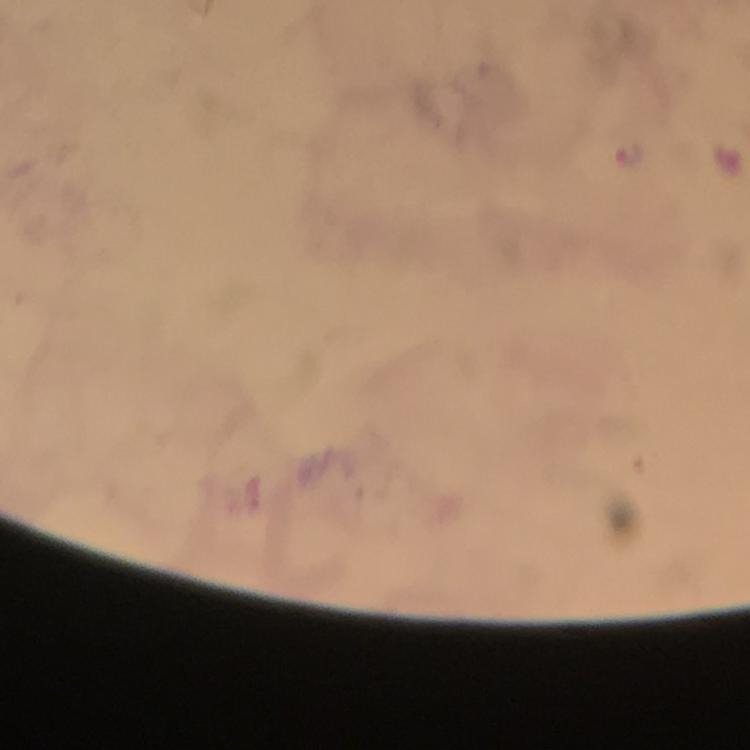

{
  "plasmodium_parasite_locations": "approximate centers as (x, y) in pixels: (630, 156)",
  "immersion_oil": "applied",
  "magnification": "100x",
  "image_size": "750×750 pixels",
  "cropped_from": "a single field of view",
  "stain": "Giemsa",
  "context": "from a diagnostic examination for malaria",
  "capture": "smartphone photograph through a microscope",
  "preparation": "thick blood film"
}